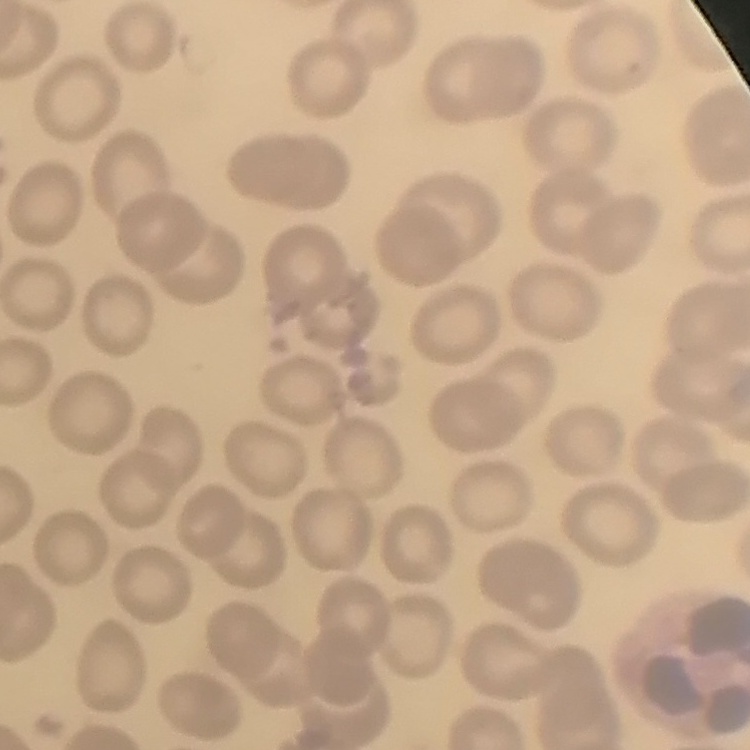 The red blood cells exhibit no rouleaux formation. Stained with either Field's or Giemsa. Thin blood film. Square crop of a larger photomicrograph.